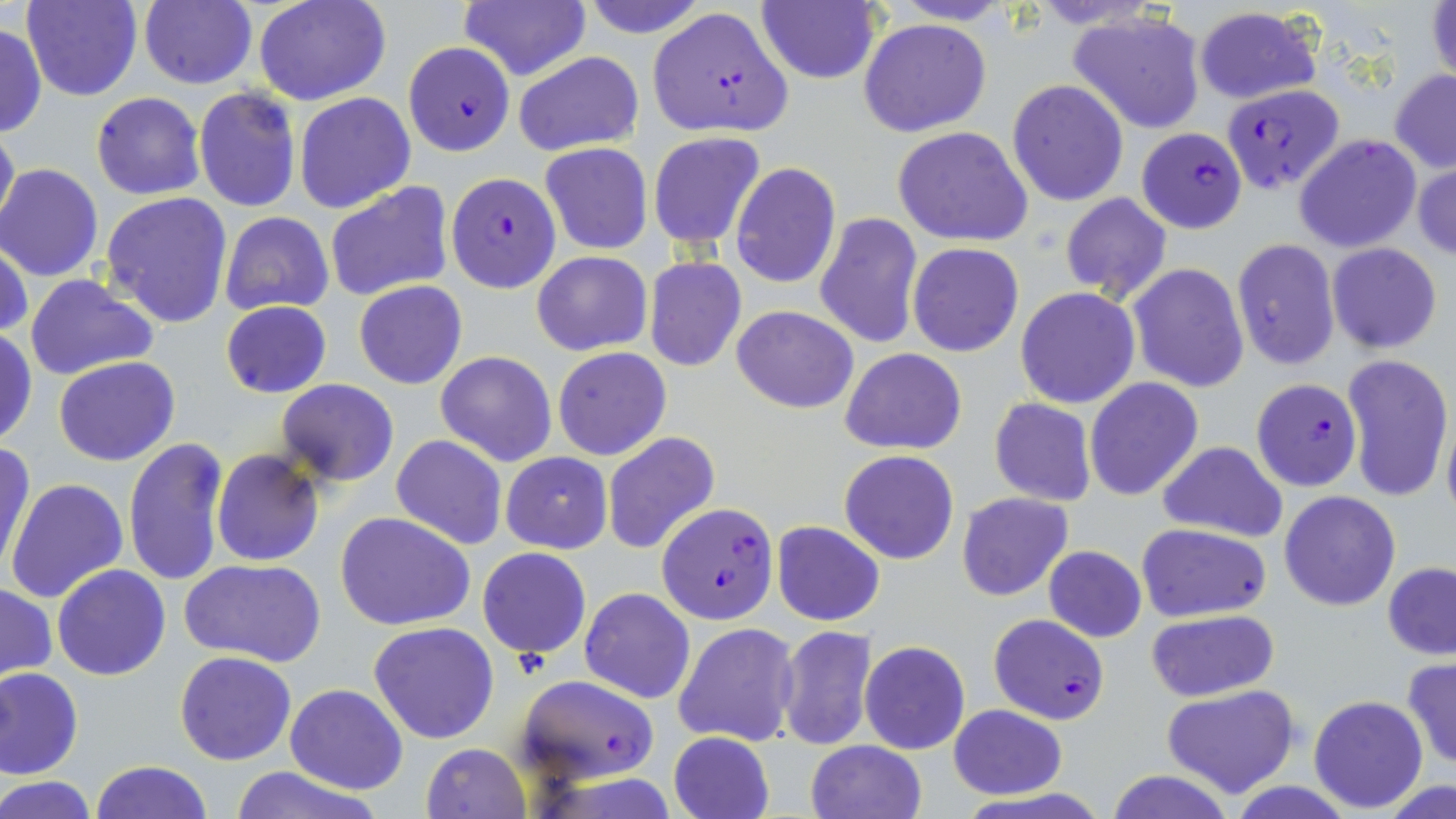
Summary:
  - Coordinate format: approximate bounding boxes as [x1, y1, x2, y2] in pixels
  - Uninfected red blood cell locations: [23, 0, 142, 102], [253, 0, 390, 106], [576, 0, 709, 38], [136, 1, 258, 88], [459, 1, 591, 82], [755, 2, 881, 85], [1426, 3, 1456, 89], [1193, 6, 1322, 103], [1068, 10, 1207, 133], [859, 18, 990, 137], [0, 22, 46, 139], [512, 51, 644, 157], [1390, 69, 1456, 173], [1006, 79, 1128, 206], [193, 88, 301, 212], [92, 91, 205, 200], [293, 93, 415, 213], [0, 118, 18, 237], [892, 126, 1033, 247], [648, 131, 766, 247], [1292, 133, 1422, 253], [539, 141, 653, 255], [1413, 155, 1456, 263], [731, 163, 841, 288], [0, 166, 103, 282], [325, 181, 453, 303], [101, 191, 234, 328], [1061, 192, 1171, 304], [219, 211, 335, 315], [815, 211, 924, 350], [1231, 238, 1341, 370], [1, 239, 32, 343], [907, 242, 1024, 356], [1326, 243, 1444, 353], [532, 251, 652, 356], [644, 255, 746, 372], [1128, 262, 1251, 393], [26, 274, 159, 381], [353, 280, 468, 389], [1015, 287, 1142, 410], [220, 301, 332, 398], [732, 304, 858, 413], [1, 329, 37, 446], [552, 345, 672, 461], [840, 348, 966, 455], [434, 351, 558, 466], [1342, 352, 1453, 503], [54, 356, 180, 466], [1083, 377, 1204, 502], [275, 379, 400, 486], [989, 398, 1097, 505], [1441, 407, 1456, 527], [601, 431, 721, 555], [390, 435, 507, 549], [122, 436, 230, 586], [357, 440, 496, 619], [1, 441, 35, 579], [1157, 441, 1288, 542], [212, 449, 324, 566], [840, 449, 959, 565], [501, 451, 613, 553], [6, 479, 128, 604], [957, 491, 1073, 601], [1280, 491, 1401, 611], [333, 511, 477, 632], [771, 521, 886, 626], [1135, 521, 1272, 621], [477, 546, 590, 659], [1043, 546, 1146, 643], [179, 558, 327, 668], [1383, 562, 1456, 659], [52, 565, 171, 681], [1, 583, 56, 680], [580, 587, 696, 704], [1145, 610, 1280, 703], [369, 621, 500, 744], [674, 622, 800, 748], [777, 625, 879, 749], [860, 640, 971, 755], [175, 650, 297, 765], [1402, 657, 1456, 770], [0, 667, 84, 779], [284, 682, 408, 795], [1160, 684, 1300, 797], [1309, 695, 1429, 813], [947, 704, 1068, 798], [667, 731, 775, 819], [806, 741, 927, 819], [421, 742, 532, 819], [91, 760, 212, 818], [228, 765, 384, 819], [1106, 769, 1236, 819], [2, 777, 96, 818], [1382, 779, 1453, 819]
  - Plasmodium falciparum-infected red blood cell locations: [649, 8, 792, 139], [403, 41, 512, 157], [1221, 83, 1344, 194], [1135, 128, 1247, 232], [446, 173, 561, 293], [1251, 377, 1363, 493], [655, 502, 779, 625], [987, 613, 1109, 724], [516, 675, 658, 784]
  - Slide-level diagnosis: Plasmodium falciparum
  - Stain: May-Grünwald-Giemsa
  - Preparation: thin blood film
  - Field of view: one of a larger specimen
  - Image size: 1456×819 pixels
  - Modality: optical microscopy
  - Magnification: 1000x